Identify the parasite.
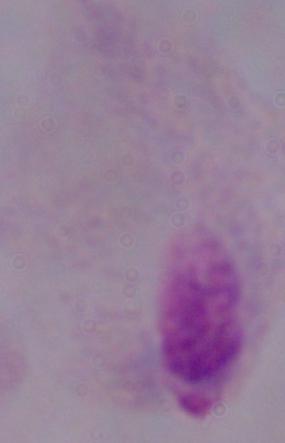

A trichomonad.

{
  "magnification": "1000x",
  "modality": "micrograph"
}